Report the malaria status of this cell.
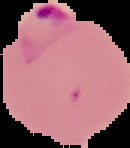
It is parasitized.

From a thin blood film. Image is 130×148 pixels. Cell region segmented out of the field of view; the surrounding area is masked to black.